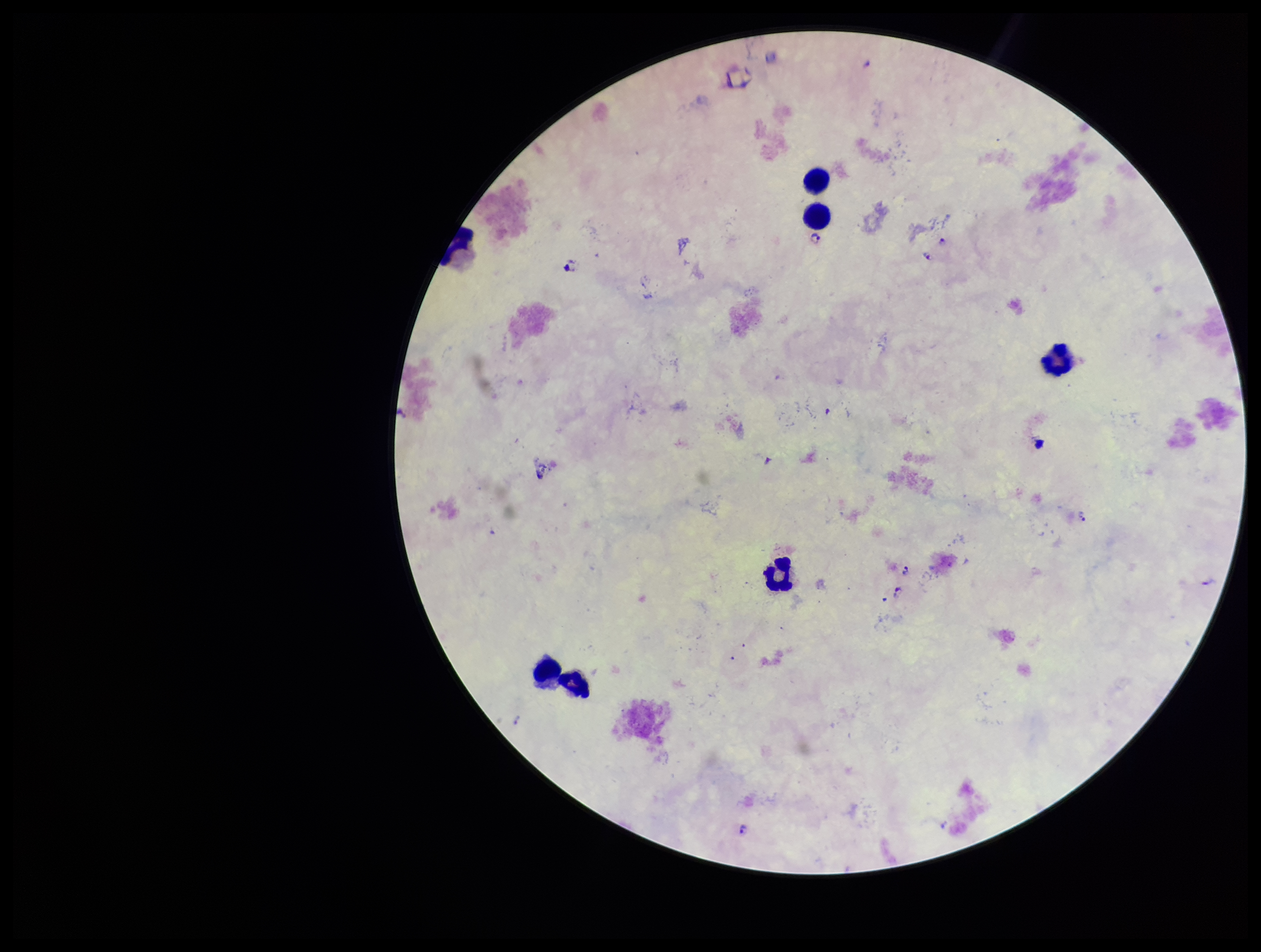

Patient malaria status: infected. Plasmodium parasites: detected. Leukocyte count: 6. Species reported for this patient: Plasmodium falciparum. Photographed through the microscope eyepiece with a smartphone camera. Preparation: thick. Image is 1261×952 pixels. One field from this slide. Parasite count: 7. Stained with Giemsa.